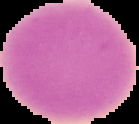

Result: negative for Plasmodium parasites. Image is 139×124 pixels. Segmented cell region on a black background. From a thin blood film.